Point out each malaria parasite and each leukocyte.
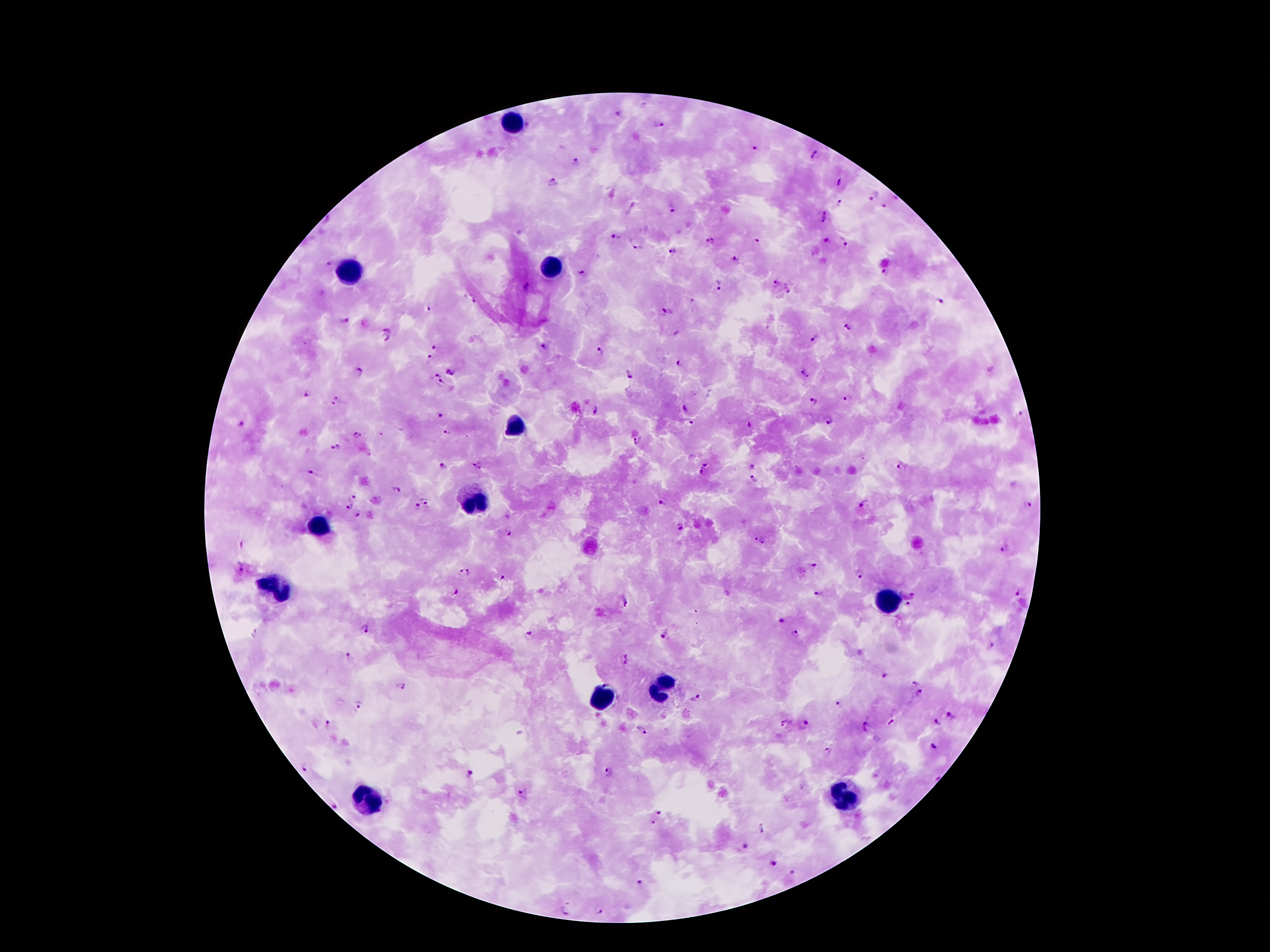
Approximate centers as {x, y} in pixels.
Malaria parasites: {619, 114}, {659, 124}, {753, 149}, {812, 155}, {575, 162}, {551, 182}, {839, 184}, {874, 196}, {893, 199}, {841, 203}, {885, 206}, {673, 209}, {824, 217}, {616, 236}, {710, 242}, {755, 242}, {825, 243}, {845, 244}, {638, 246}, {673, 251}, {735, 259}, {328, 264}, {582, 273}, {885, 273}, {778, 282}, {721, 285}, {528, 287}, {788, 290}, {473, 301}, {693, 301}, {940, 302}, {429, 308}, {667, 309}, {345, 320}, {848, 327}, {390, 328}, {815, 339}, {385, 340}, {436, 346}, {545, 347}, {601, 352}, {430, 358}, {679, 363}, {452, 370}, {360, 372}, {630, 374}, {434, 375}, {804, 375}, {444, 384}, {306, 393}, {338, 397}, {847, 398}, {813, 402}, {333, 404}, {684, 409}, {597, 410}, {440, 414}, {1019, 414}, {691, 422}, {831, 422}, {241, 425}, {750, 426}, {447, 432}, {358, 435}, {638, 441}, {335, 447}, {707, 463}, {443, 465}, {477, 465}, {752, 467}, {902, 467}, {702, 472}, {312, 473}, {755, 479}, {396, 490}, {350, 497}, {425, 499}, {663, 503}, {865, 503}, {1030, 504}, {349, 507}, {417, 507}, {358, 514}, {681, 527}, {507, 531}, {755, 538}, {763, 542}, {245, 547}, {1004, 549}, {814, 565}, {241, 568}, {471, 572}, {860, 572}, {461, 573}, {502, 577}, {456, 591}, {913, 593}, {1019, 593}, {819, 594}, {627, 600}, {907, 605}, {782, 620}, {365, 631}, {794, 632}, {255, 633}, {531, 633}, {666, 634}, {991, 645}, {350, 656}, {627, 659}, {884, 675}, {916, 682}, {400, 686}, {921, 691}, {697, 698}, {358, 703}, {839, 704}, {952, 716}, {939, 721}, {783, 722}, {891, 722}, {328, 723}, {803, 724}, {867, 724}, {641, 730}, {934, 746}, {830, 750}, {306, 767}, {610, 771}, {469, 773}, {524, 795}, {333, 806}, {659, 813}, {653, 821}, {762, 829}, {745, 846}, {775, 864}, {792, 872}, {639, 881}, {565, 909}, {599, 911}.
Leukocytes: {514, 125}, {553, 264}, {349, 272}, {515, 427}, {477, 503}, {320, 526}, {274, 587}, {888, 600}, {659, 686}, {602, 700}, {368, 800}, {846, 800}.

Summary:
  - Capture: smartphone through the microscope eyepiece
  - Preparation: thick peripheral-blood smear
  - Field of view: one from this slide
  - Magnification: 100x
  - Image size: 1270×952 pixels
  - Patient malaria status: positive for Plasmodium falciparum
  - Stain: Giemsa